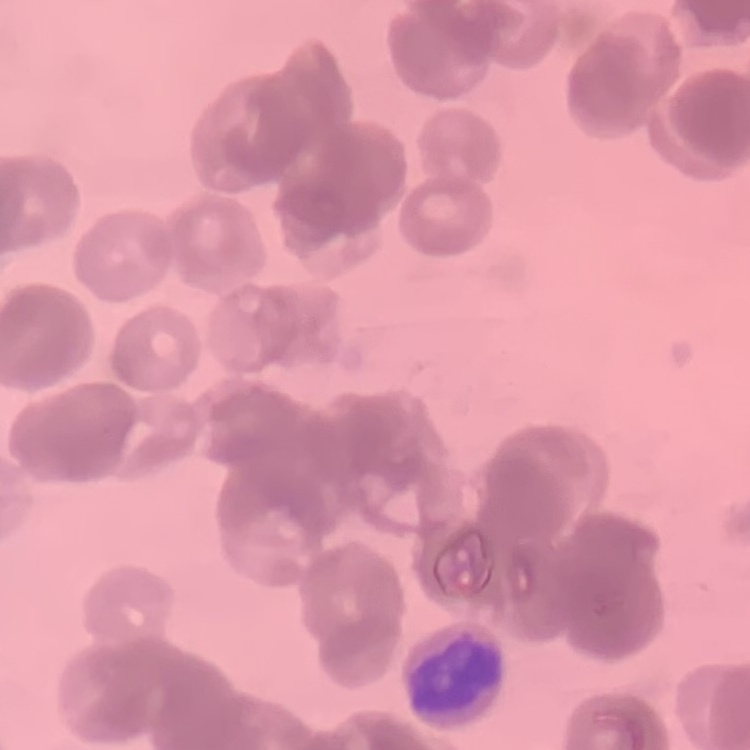
The erythrocytes exhibit rouleaux formation. Thin peripheral smear. Stained with either Field's or Giemsa. Square crop of a larger photomicrograph.